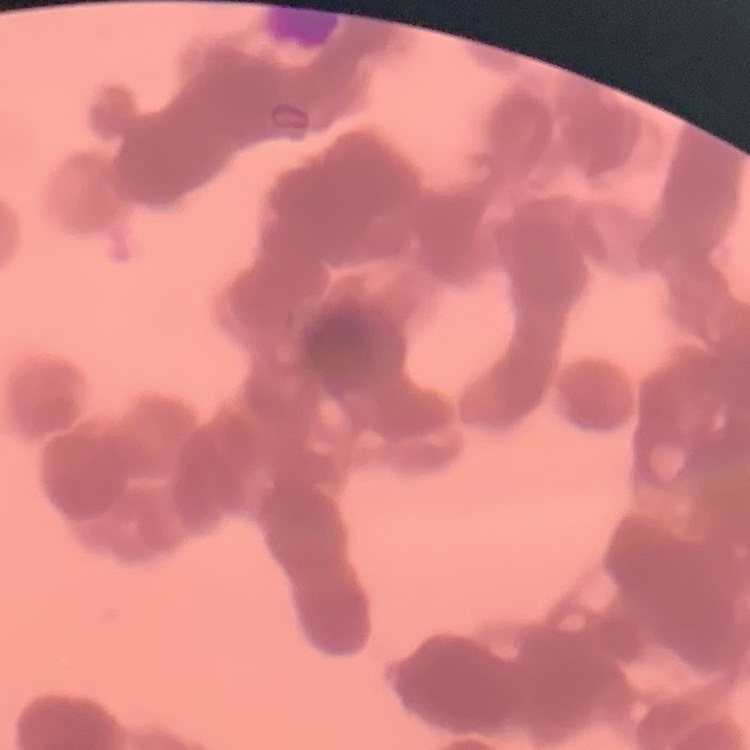
red_blood_cell_morphology: rouleaux formation
stain: Field's or Giemsa
image_type: square crop of a larger photomicrograph
preparation: thin peripheral smear